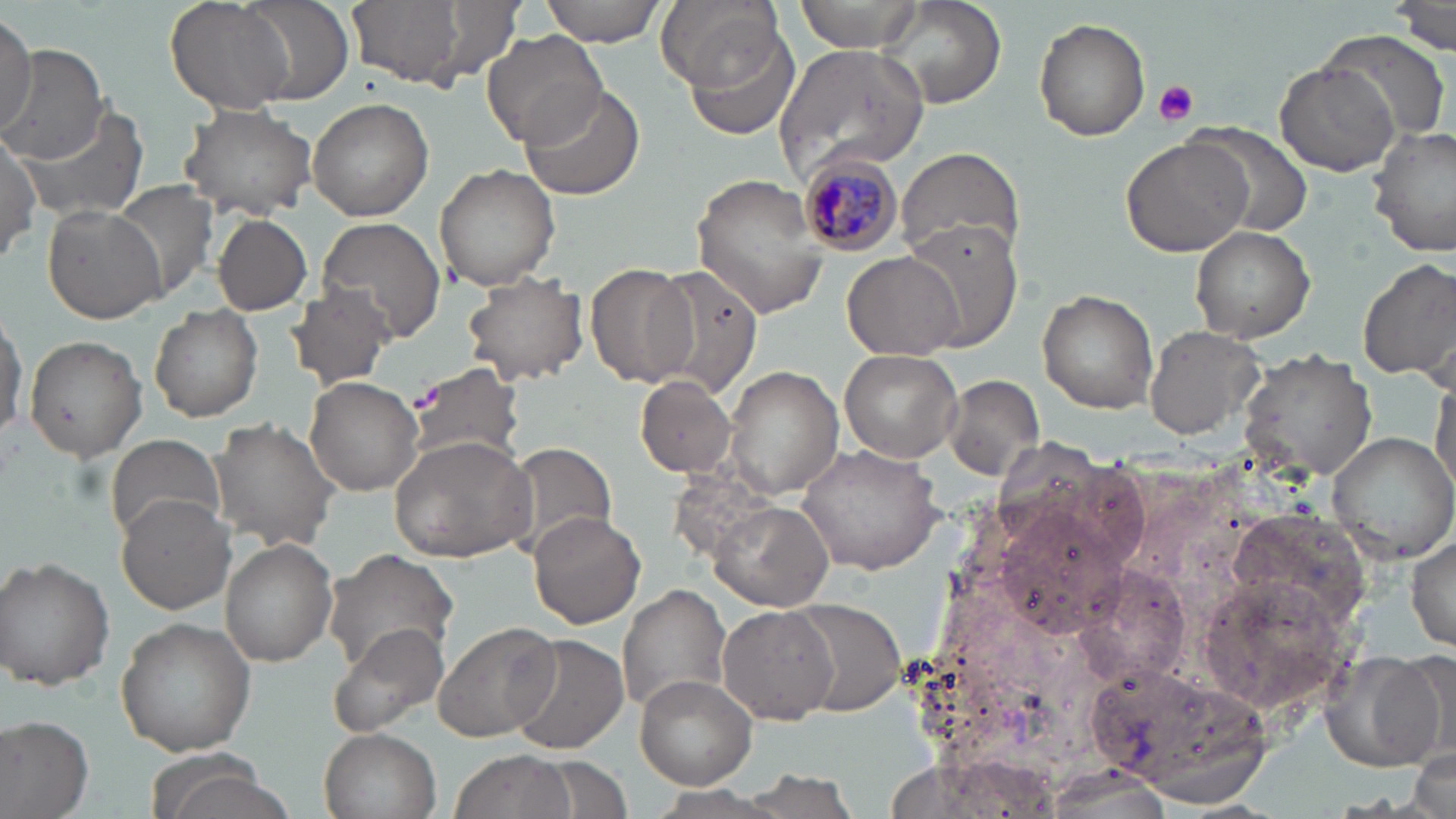 Approximate bounding boxes as [x1, y1, x2, y2] in pixels. Uninfected red blood cell locations: [165, 0, 295, 114], [237, 0, 353, 105], [346, 0, 490, 89], [539, 0, 664, 45], [658, 0, 784, 90], [793, 0, 927, 53], [879, 1, 1006, 110], [1391, 1, 1456, 54], [0, 10, 38, 133], [1033, 17, 1151, 141], [682, 24, 803, 142], [478, 30, 606, 150], [1324, 30, 1452, 140], [773, 42, 932, 180], [0, 46, 110, 165], [1274, 59, 1398, 178], [519, 83, 646, 202], [308, 97, 434, 220], [177, 103, 320, 218], [15, 104, 148, 222], [1188, 120, 1312, 238], [1368, 124, 1456, 258], [0, 131, 41, 264], [1120, 135, 1252, 259], [894, 146, 1026, 262], [435, 163, 560, 290], [689, 172, 827, 319], [111, 181, 220, 302], [41, 203, 163, 324], [210, 212, 313, 315], [316, 217, 446, 341], [900, 222, 1021, 348], [1191, 227, 1316, 342], [844, 251, 961, 358], [1357, 255, 1454, 384], [585, 261, 698, 390], [651, 263, 764, 395], [461, 273, 589, 387], [284, 286, 398, 392], [1037, 288, 1159, 412], [150, 305, 264, 422], [0, 311, 27, 442], [1143, 325, 1268, 441], [23, 334, 147, 461], [838, 347, 964, 463], [1237, 347, 1377, 482], [401, 361, 525, 470], [725, 364, 844, 501], [1431, 373, 1455, 500], [636, 374, 737, 478], [302, 376, 423, 497], [944, 376, 1043, 479], [208, 418, 337, 552], [1326, 431, 1456, 563], [103, 434, 224, 545], [390, 436, 536, 562], [504, 441, 619, 556], [796, 441, 946, 574], [116, 495, 237, 613], [712, 501, 834, 611], [528, 511, 645, 628], [1406, 532, 1456, 649], [219, 539, 339, 664], [324, 548, 461, 677], [2, 556, 116, 689], [1078, 565, 1191, 684], [1194, 574, 1356, 714], [617, 583, 731, 718], [789, 598, 908, 717], [718, 606, 841, 724], [114, 616, 258, 757], [433, 621, 560, 741], [329, 625, 450, 736], [507, 634, 630, 755], [1338, 649, 1454, 769], [1090, 654, 1270, 798], [634, 675, 756, 788], [0, 713, 94, 819], [319, 727, 441, 819], [1410, 747, 1453, 819], [450, 750, 578, 819], [141, 754, 284, 819], [536, 756, 630, 814]. Platelet locations: [1152, 79, 1201, 126]. Plasmodium malariae-infected red blood cell locations: [794, 152, 904, 259]. Slide-level diagnosis: Plasmodium malariae. Light microscopy. 1000x magnification. Single field of view. May-Grünwald-Giemsa stain. Thin blood film. Image is 1456×819 pixels.